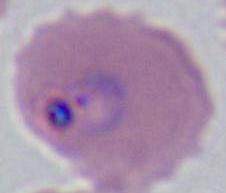
Photomicrograph. 400x or 1000x magnification. A Plasmodium parasite is shown.